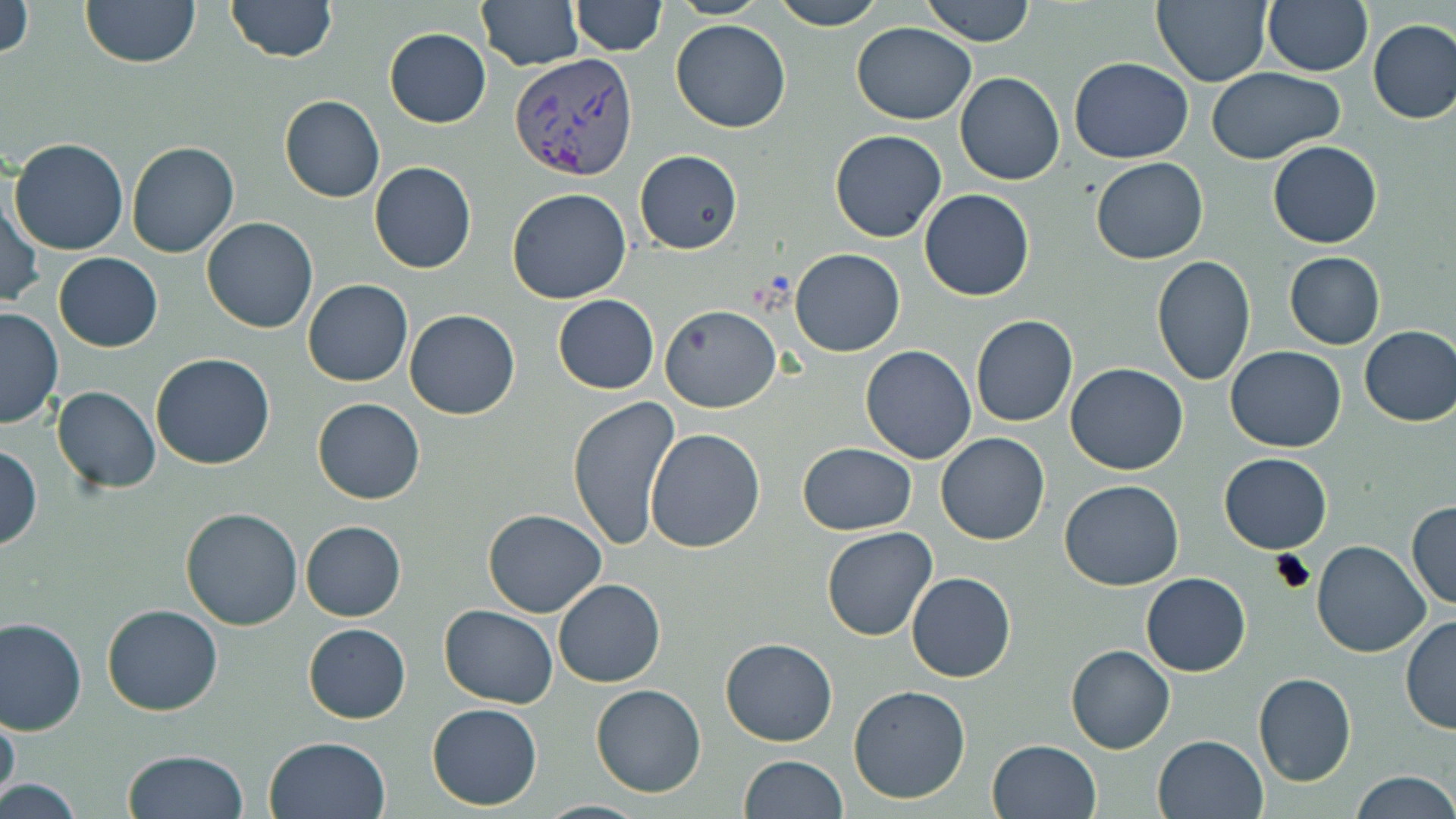
slide-level diagnosis = Plasmodium vivax
preparation = thin blood film
field of view = one of a larger specimen
magnification = 1000x
image size = 1456×819 pixels
modality = light microscopy
Plasmodium vivax-infected red blood cell locations = approximate bounding boxes as named x1/y1/x2/y2 corners in pixels: (x1=508, y1=52, x2=639, y2=179)
uninfected red blood cell locations = approximate bounding boxes as named x1/y1/x2/y2 corners in pixels: (x1=0, y1=0, x2=34, y2=60), (x1=80, y1=0, x2=202, y2=69), (x1=225, y1=0, x2=337, y2=64), (x1=476, y1=0, x2=583, y2=71), (x1=667, y1=0, x2=771, y2=20), (x1=773, y1=0, x2=884, y2=28), (x1=921, y1=0, x2=1036, y2=46), (x1=1152, y1=0, x2=1272, y2=86), (x1=571, y1=1, x2=665, y2=56), (x1=1263, y1=1, x2=1372, y2=76), (x1=1368, y1=18, x2=1456, y2=124), (x1=669, y1=20, x2=792, y2=133), (x1=851, y1=22, x2=977, y2=124), (x1=384, y1=28, x2=491, y2=128), (x1=1069, y1=57, x2=1194, y2=164), (x1=1206, y1=67, x2=1345, y2=163), (x1=955, y1=72, x2=1063, y2=185), (x1=279, y1=96, x2=385, y2=203), (x1=829, y1=130, x2=946, y2=242), (x1=9, y1=137, x2=129, y2=255), (x1=126, y1=140, x2=238, y2=258), (x1=1267, y1=141, x2=1382, y2=249), (x1=633, y1=149, x2=743, y2=254), (x1=1091, y1=157, x2=1208, y2=265), (x1=368, y1=161, x2=477, y2=274), (x1=506, y1=187, x2=632, y2=304), (x1=919, y1=188, x2=1035, y2=301), (x1=1, y1=191, x2=43, y2=309), (x1=201, y1=217, x2=318, y2=333), (x1=789, y1=249, x2=905, y2=357), (x1=53, y1=252, x2=163, y2=352), (x1=1283, y1=252, x2=1385, y2=349), (x1=1150, y1=254, x2=1257, y2=386), (x1=302, y1=279, x2=413, y2=387), (x1=553, y1=295, x2=659, y2=393), (x1=658, y1=305, x2=780, y2=413), (x1=0, y1=307, x2=63, y2=429), (x1=404, y1=308, x2=521, y2=421), (x1=970, y1=315, x2=1078, y2=428), (x1=1358, y1=325, x2=1456, y2=427), (x1=860, y1=345, x2=978, y2=464), (x1=1225, y1=346, x2=1346, y2=452), (x1=151, y1=353, x2=275, y2=470), (x1=1064, y1=364, x2=1189, y2=475), (x1=51, y1=386, x2=161, y2=495), (x1=567, y1=394, x2=681, y2=553), (x1=312, y1=397, x2=424, y2=504), (x1=645, y1=427, x2=765, y2=552), (x1=935, y1=431, x2=1050, y2=546), (x1=797, y1=442, x2=917, y2=535), (x1=0, y1=444, x2=42, y2=551), (x1=1220, y1=453, x2=1332, y2=554), (x1=1060, y1=479, x2=1184, y2=589), (x1=1406, y1=502, x2=1456, y2=610), (x1=179, y1=507, x2=305, y2=631), (x1=482, y1=508, x2=608, y2=617), (x1=299, y1=520, x2=406, y2=621), (x1=821, y1=527, x2=937, y2=642), (x1=1313, y1=540, x2=1429, y2=657), (x1=906, y1=572, x2=1016, y2=682), (x1=1140, y1=572, x2=1252, y2=676), (x1=553, y1=578, x2=666, y2=688), (x1=100, y1=604, x2=223, y2=716), (x1=439, y1=604, x2=558, y2=709), (x1=0, y1=617, x2=87, y2=735), (x1=1400, y1=617, x2=1456, y2=734), (x1=303, y1=623, x2=411, y2=722), (x1=721, y1=638, x2=837, y2=747), (x1=1066, y1=643, x2=1175, y2=755), (x1=1253, y1=672, x2=1357, y2=787), (x1=847, y1=683, x2=972, y2=804), (x1=591, y1=684, x2=707, y2=798), (x1=426, y1=702, x2=543, y2=810), (x1=1, y1=705, x2=20, y2=808), (x1=1153, y1=734, x2=1270, y2=819), (x1=263, y1=735, x2=391, y2=819), (x1=987, y1=739, x2=1102, y2=819), (x1=122, y1=749, x2=249, y2=819), (x1=739, y1=755, x2=848, y2=818), (x1=1351, y1=772, x2=1455, y2=818), (x1=4, y1=774, x2=83, y2=819), (x1=537, y1=800, x2=651, y2=818)
stain = May-Grünwald-Giemsa